Comment on the morphology of the erythrocytes.
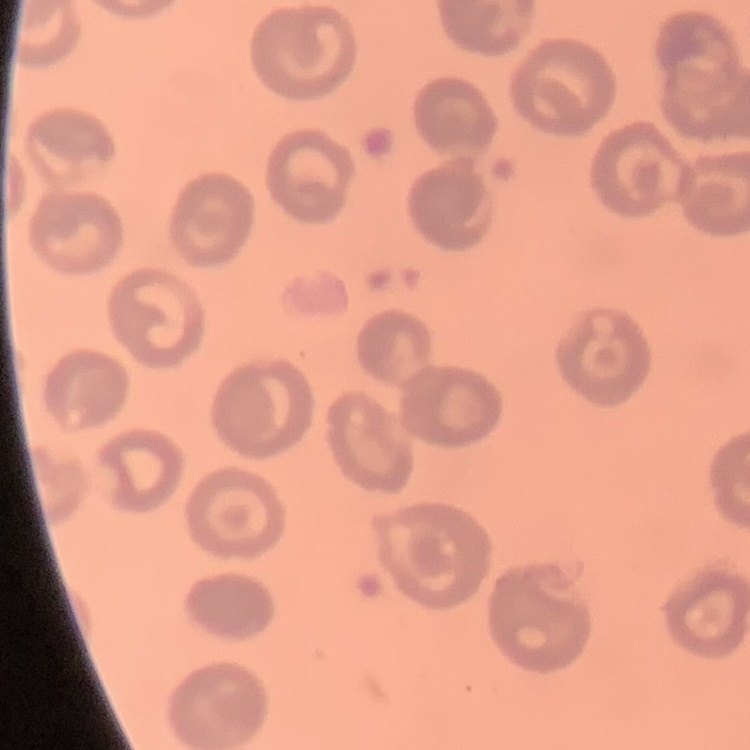
They show no rouleaux formation.

Summary:
  - Stain: Field's or Giemsa
  - Preparation: thin blood smear
  - Image type: square crop of a larger photomicrograph